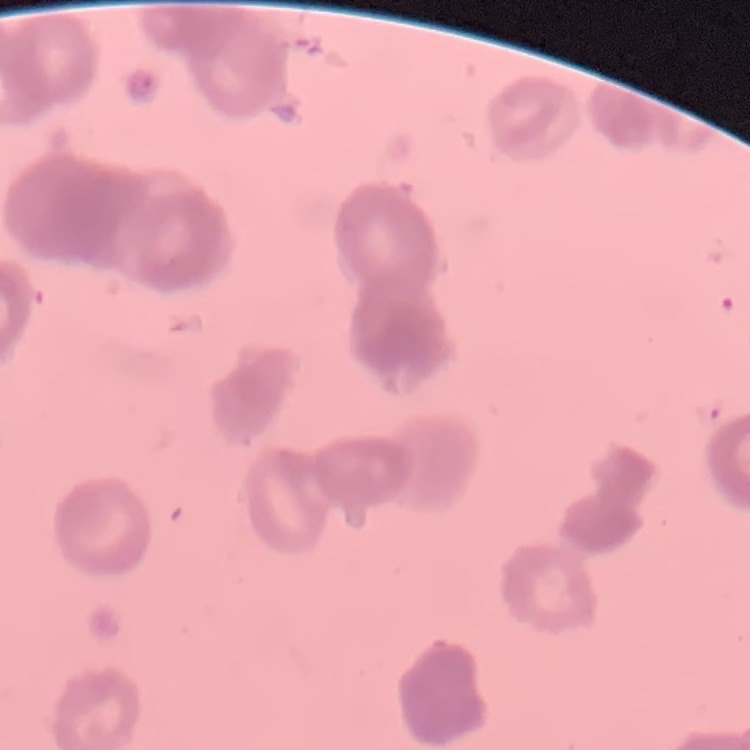

The erythrocytes exhibit rouleaux formation. Thin blood film. Field's or Giemsa stain. Square crop of a larger photomicrograph.